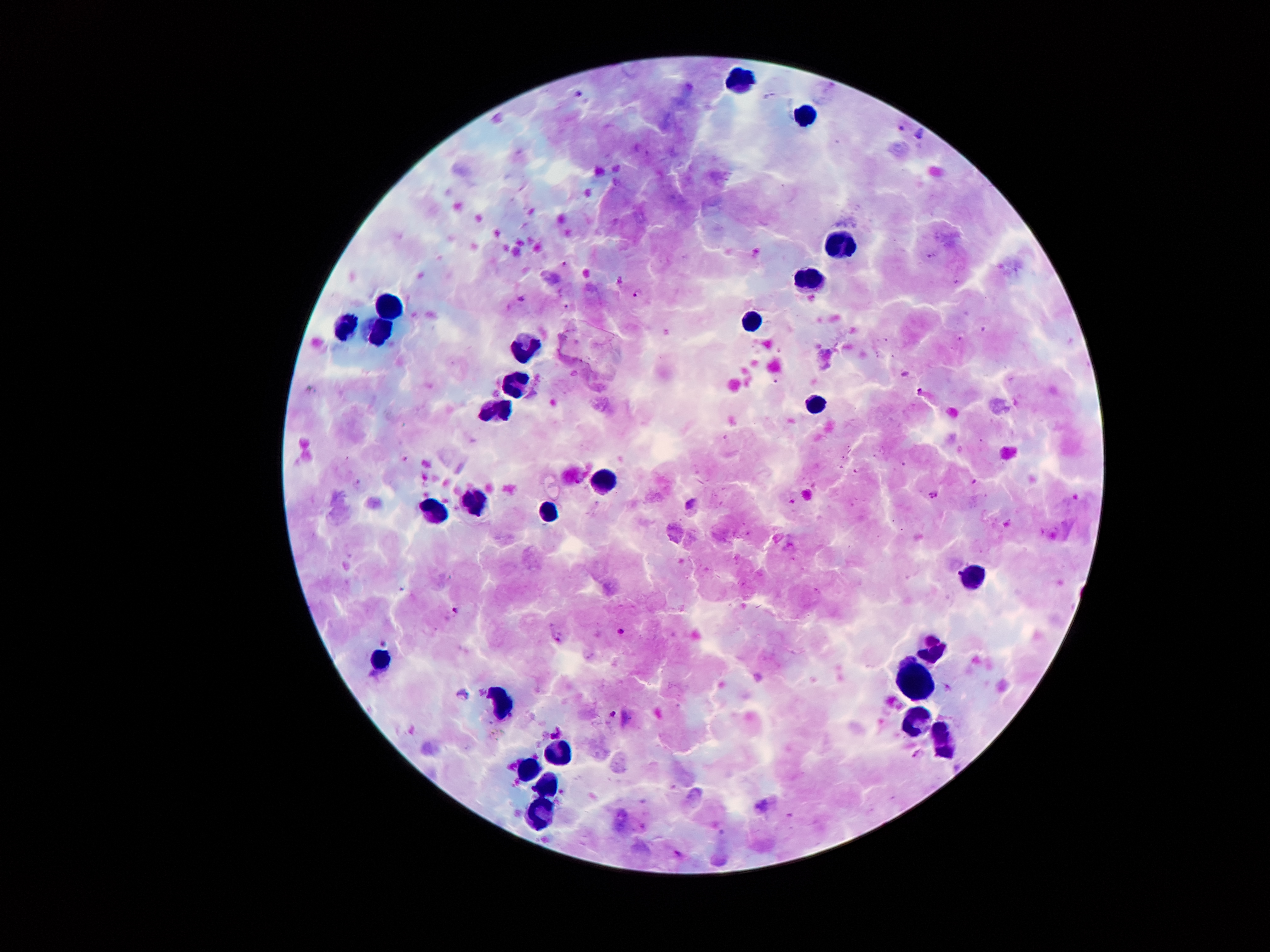
Approximate centers as (x, y) in pixels.
Summary:
  - Malaria parasite locations: (580, 92), (902, 126), (566, 263), (638, 292), (919, 390), (935, 494), (691, 501), (455, 610), (622, 632), (613, 712)
  - Leukocyte locations: (737, 78), (805, 115), (840, 245), (809, 280), (389, 302), (751, 320), (346, 326), (381, 333), (522, 348), (518, 381), (815, 405), (494, 413), (603, 477), (472, 502), (435, 510), (550, 513), (976, 578), (934, 647), (383, 659), (911, 681), (505, 707), (915, 716), (943, 741), (556, 754), (525, 768), (544, 786), (539, 814)
  - Patient malaria status: infected with Plasmodium falciparum
  - Preparation: thick blood smear
  - Field of view: single
  - Stain: Giemsa
  - Capture: smartphone camera through the microscope eyepiece
  - Magnification: 100x
  - Image size: 1270×952 pixels